Report the malaria status of this cell.
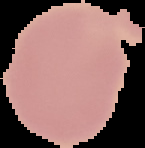
It is uninfected.

Image is 145×148 pixels. Cell region segmented out of the field of view; the surrounding area is masked to black. From a thin blood smear.